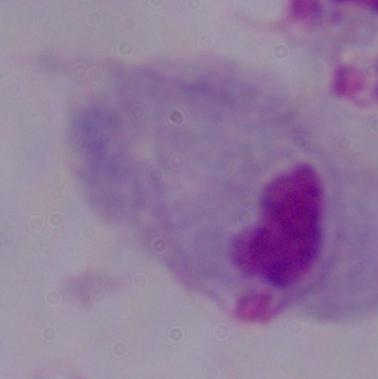

Summary:
  - Magnification: 1000x
  - Modality: photomicrograph
  - Identification: trichomonad